Describe the morphology of the red blood cells.
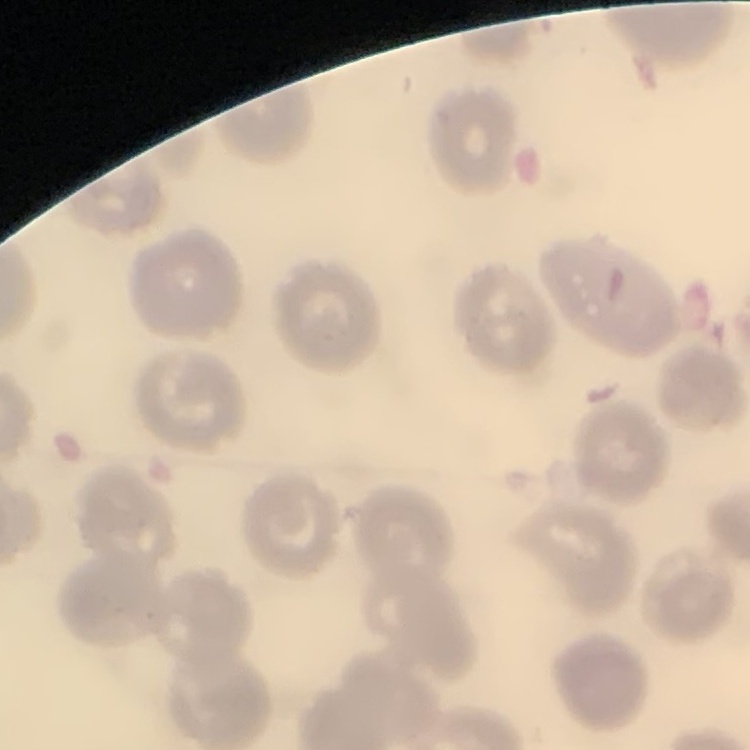
No rouleaux formation.

{
  "preparation": "thin blood smear",
  "stain": "Field's or Giemsa",
  "image_type": "one tile cut from a larger photomicrograph"
}